Evaluate for parasitized red blood cells.
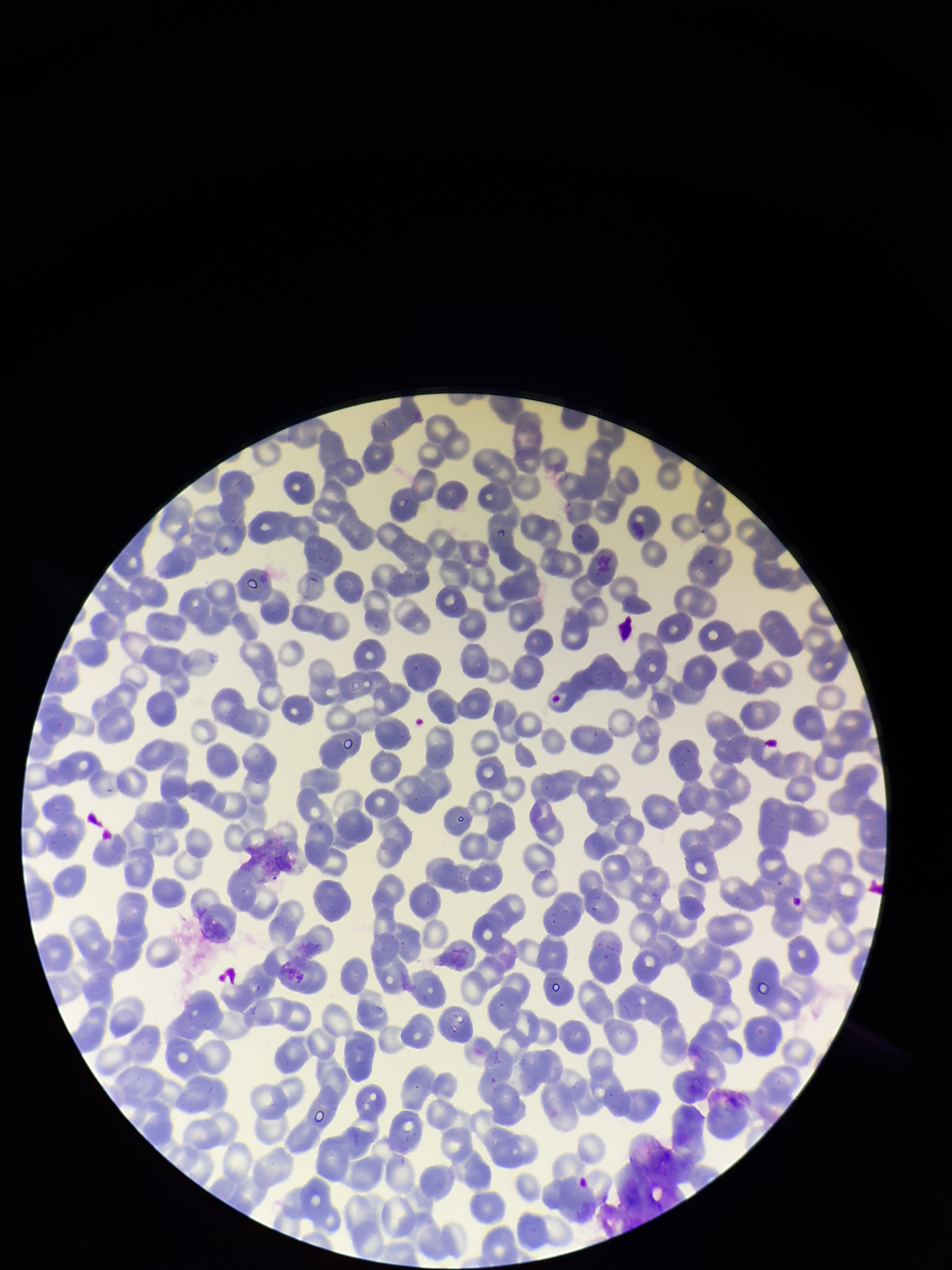

None identified.

Parasitized red blood cell count: 0. Image is 952×1270 pixels. Patient malaria status: negative. One field from this slide. Photographed through the microscope eyepiece with a smartphone camera. Red blood cell count: 272. Stained with Giemsa. Preparation: thin smear.